Identify the parasite.
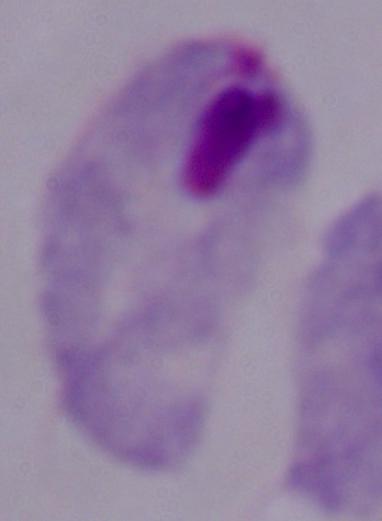
A trichomonad.

Captured at 1000x magnification. Micrograph.